Locate every leukocyte (white blood cell).
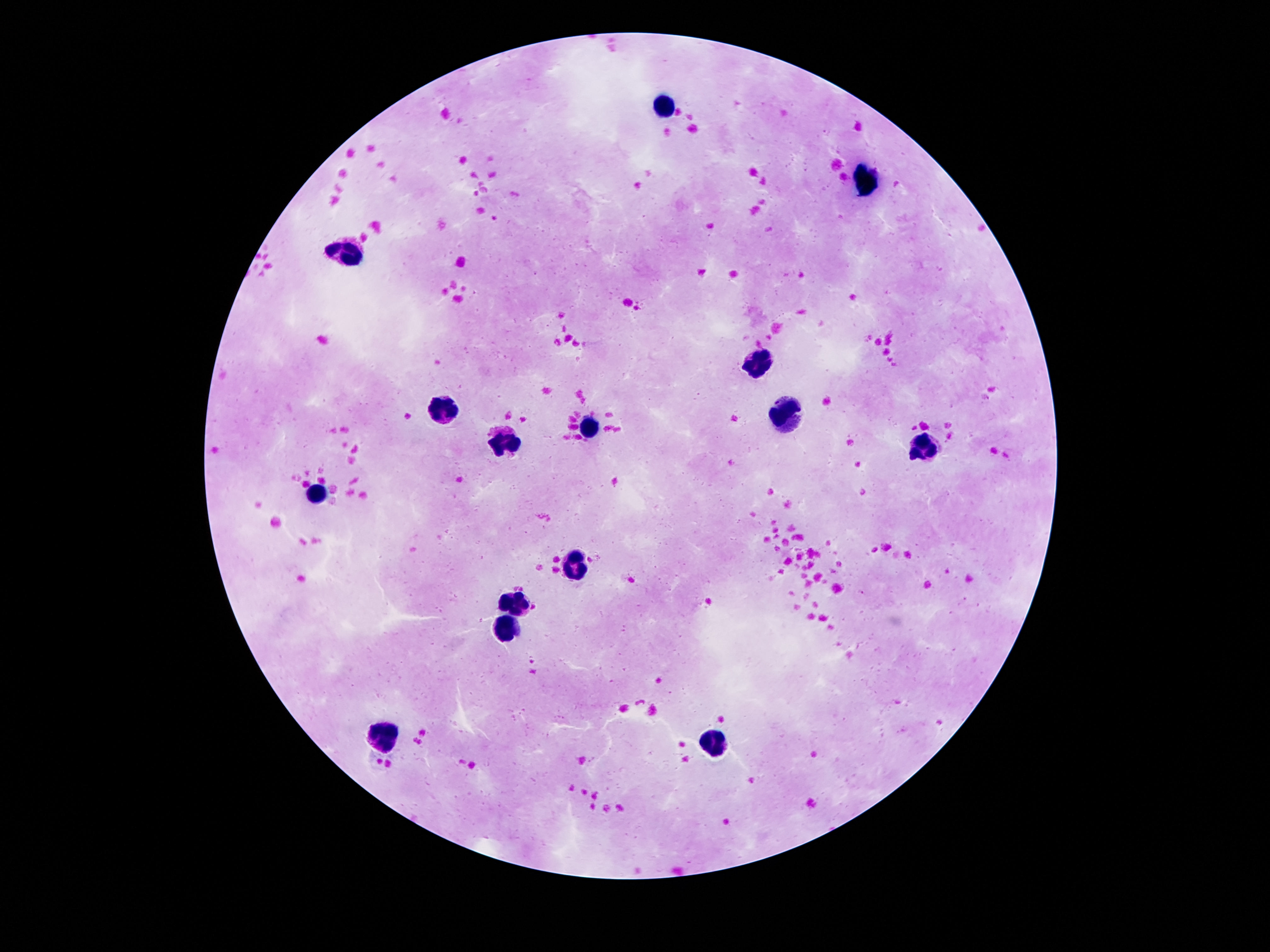
Approximate centers as [x, y] in pixels.
Leukocytes: [667, 107], [869, 181], [345, 254], [759, 360], [439, 404], [783, 417], [587, 424], [505, 445], [927, 445], [319, 495], [575, 565], [515, 597], [509, 629], [387, 735], [709, 744].

stain = Giemsa
capture = smartphone camera through the microscope eyepiece
magnification = 100x
field of view = one from this slide
preparation = thick peripheral-blood smear
patient malaria status = uninfected
image size = 1270×952 pixels